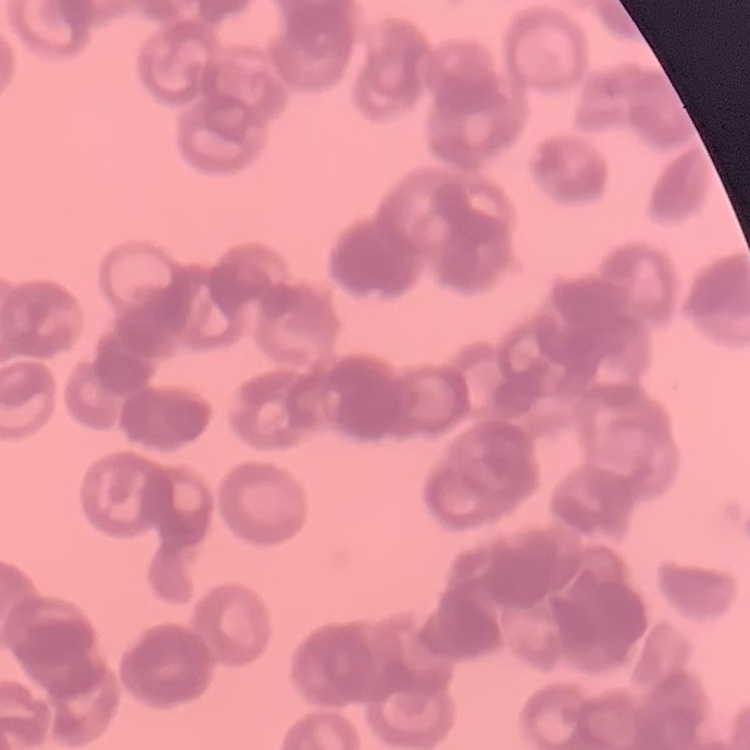
Summary:
  - Erythrocyte morphology: rouleaux formation
  - Stain: Field's or Giemsa
  - Preparation: thin peripheral smear
  - Image type: one tile cut from a larger photomicrograph